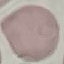
Result: no malaria parasites detected. Automatically extracted cell patch, resized to 64 × 64 pixels. Giemsa-stained preparation. Acquired by smartphone through the microscope eyepiece. Thin blood smear.